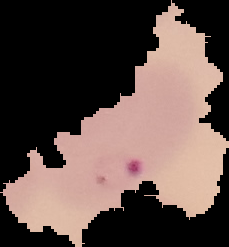 Image is 229×247 pixels. Result: malaria parasites detected. Cell region segmented out of the field of view; the surrounding area is masked to black. From a thin blood film.